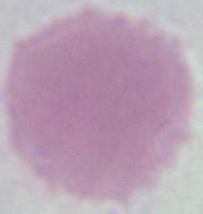

identification = red blood cell
magnification = 1000x
modality = photomicrograph